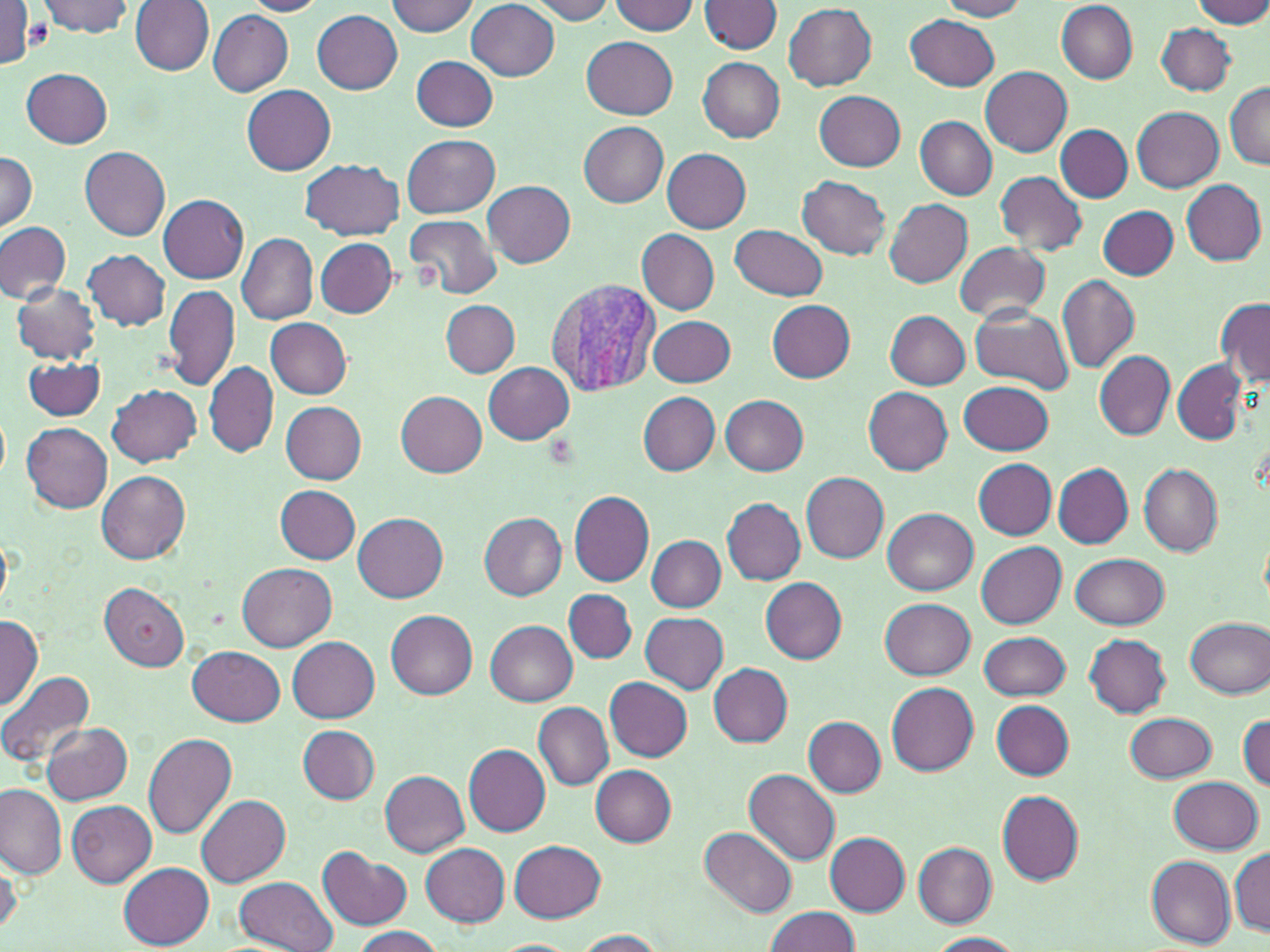

slide-level diagnosis = Plasmodium vivax
uninfected red blood cell locations = approximate bounding boxes as (x1, y1, x2, y2) in pixels: (36, 0, 134, 37), (130, 0, 215, 76), (386, 0, 479, 36), (526, 0, 616, 23), (938, 0, 1029, 20), (1193, 0, 1270, 29), (241, 1, 327, 17), (467, 1, 560, 80), (607, 1, 699, 35), (699, 1, 783, 55), (784, 3, 878, 89), (1057, 3, 1137, 83), (0, 5, 39, 71), (207, 9, 294, 95), (313, 10, 403, 94), (905, 15, 1001, 91), (1156, 23, 1235, 95), (581, 35, 679, 118), (411, 55, 498, 130), (698, 57, 785, 143), (980, 66, 1073, 154), (23, 68, 113, 148), (1224, 81, 1270, 170), (242, 85, 336, 175), (813, 91, 906, 171), (1133, 107, 1224, 192), (915, 117, 998, 198), (579, 122, 669, 207), (1056, 125, 1132, 202), (404, 135, 500, 218), (80, 146, 171, 241), (662, 148, 751, 231), (0, 151, 39, 232), (300, 158, 405, 240), (994, 170, 1087, 256), (797, 176, 891, 259), (1181, 179, 1267, 266), (483, 181, 575, 267), (158, 195, 248, 283), (884, 198, 973, 288), (1098, 206, 1178, 278), (405, 214, 500, 300), (0, 221, 72, 304), (731, 224, 828, 299), (636, 230, 719, 315), (237, 233, 319, 324), (314, 236, 399, 318), (955, 243, 1051, 322), (84, 250, 171, 330), (1058, 274, 1139, 374), (12, 283, 100, 364), (164, 283, 241, 392), (1216, 298, 1270, 385), (442, 300, 521, 376), (767, 300, 856, 383), (968, 308, 1075, 395), (885, 311, 970, 389), (649, 315, 736, 387), (266, 317, 351, 398), (1094, 351, 1174, 440), (23, 357, 107, 418), (204, 361, 279, 456), (1172, 361, 1248, 444), (484, 362, 574, 445), (960, 382, 1055, 454), (107, 384, 201, 465), (864, 387, 953, 475), (395, 390, 488, 476), (639, 392, 719, 476), (721, 394, 809, 476), (280, 399, 367, 484), (22, 422, 113, 513), (972, 458, 1057, 538), (1053, 463, 1132, 547), (1139, 464, 1222, 556), (97, 470, 191, 564), (803, 472, 888, 562), (276, 485, 360, 564), (568, 489, 654, 586), (723, 498, 806, 584), (883, 508, 976, 594), (354, 513, 448, 602), (479, 513, 566, 600), (0, 534, 15, 610), (648, 535, 725, 611), (975, 540, 1066, 628), (1072, 554, 1169, 628), (236, 561, 335, 651), (760, 577, 847, 663), (99, 582, 189, 671), (565, 588, 637, 663), (881, 599, 976, 679), (387, 610, 477, 699), (641, 612, 728, 694), (0, 615, 43, 710), (1185, 615, 1270, 699), (486, 621, 577, 706), (977, 630, 1070, 701), (1084, 635, 1172, 717), (288, 637, 379, 722), (189, 645, 285, 726), (709, 662, 792, 747), (0, 670, 96, 769), (604, 677, 693, 760), (886, 682, 979, 773), (992, 702, 1075, 780), (534, 703, 613, 789), (1124, 711, 1216, 782), (1238, 714, 1270, 792), (804, 716, 887, 797), (40, 722, 133, 804), (298, 726, 381, 802), (144, 733, 238, 839), (463, 745, 550, 835), (590, 766, 675, 846), (744, 769, 840, 865), (380, 770, 468, 857), (1170, 776, 1262, 854), (1, 784, 67, 879), (995, 789, 1083, 886), (197, 794, 290, 887), (66, 799, 156, 888), (700, 828, 796, 916), (825, 832, 911, 915), (510, 840, 607, 923), (914, 842, 997, 926), (422, 843, 511, 926), (319, 848, 412, 931), (1230, 849, 1270, 935), (1193, 851, 1268, 944), (0, 852, 21, 937), (1145, 854, 1238, 949), (119, 862, 214, 948), (233, 875, 337, 952), (765, 906, 861, 952), (350, 926, 444, 951), (572, 929, 667, 950), (924, 933, 1025, 952), (485, 939, 580, 951)
magnification = 1000x
modality = optical microscopy
Plasmodium vivax-infected red blood cell locations = approximate bounding boxes as (x1, y1, x2, y2) in pixels: (547, 275, 660, 396)
preparation = thin blood smear
stain = May-Grünwald-Giemsa
field of view = one of a larger specimen
platelet locations = approximate bounding boxes as (x1, y1, x2, y2) in pixels: (16, 18, 52, 54)
image size = 1270×952 pixels